State which cell type is depicted.
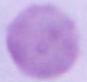
This is an erythrocyte.

magnification = 1000x
modality = photomicrograph